Report the malaria status of this cell.
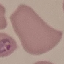

It is parasitized.

Summary:
  - Capture: smartphone through the microscope eyepiece
  - Image type: automatically extracted cell patch, resized to 64 × 64 pixels
  - Preparation: thin blood film
  - Stain: Giemsa